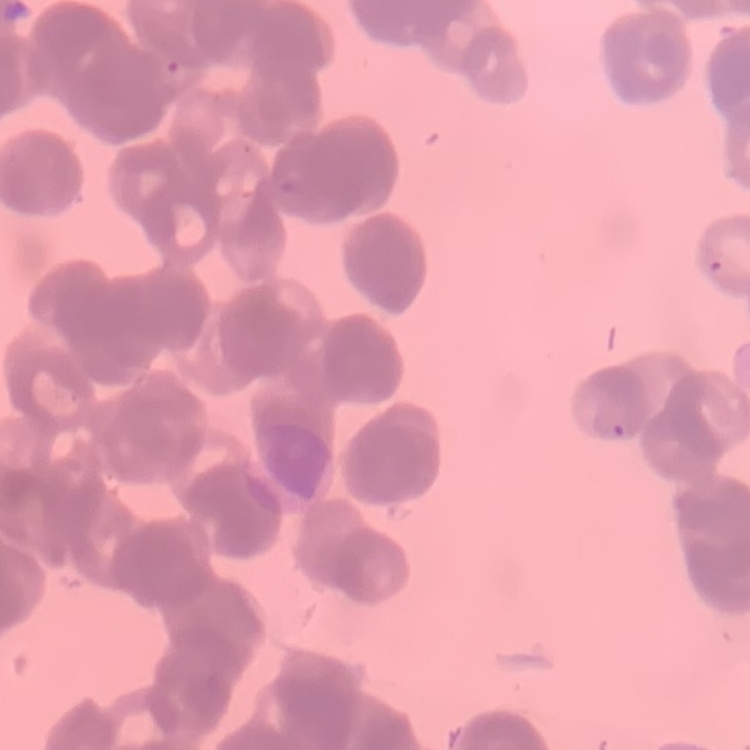

Summary:
  - Red blood cell morphology: rouleaux formation
  - Preparation: thin blood film
  - Image type: square crop of a larger photomicrograph
  - Stain: Field's or Giemsa